Locate every Plasmodium parasite.
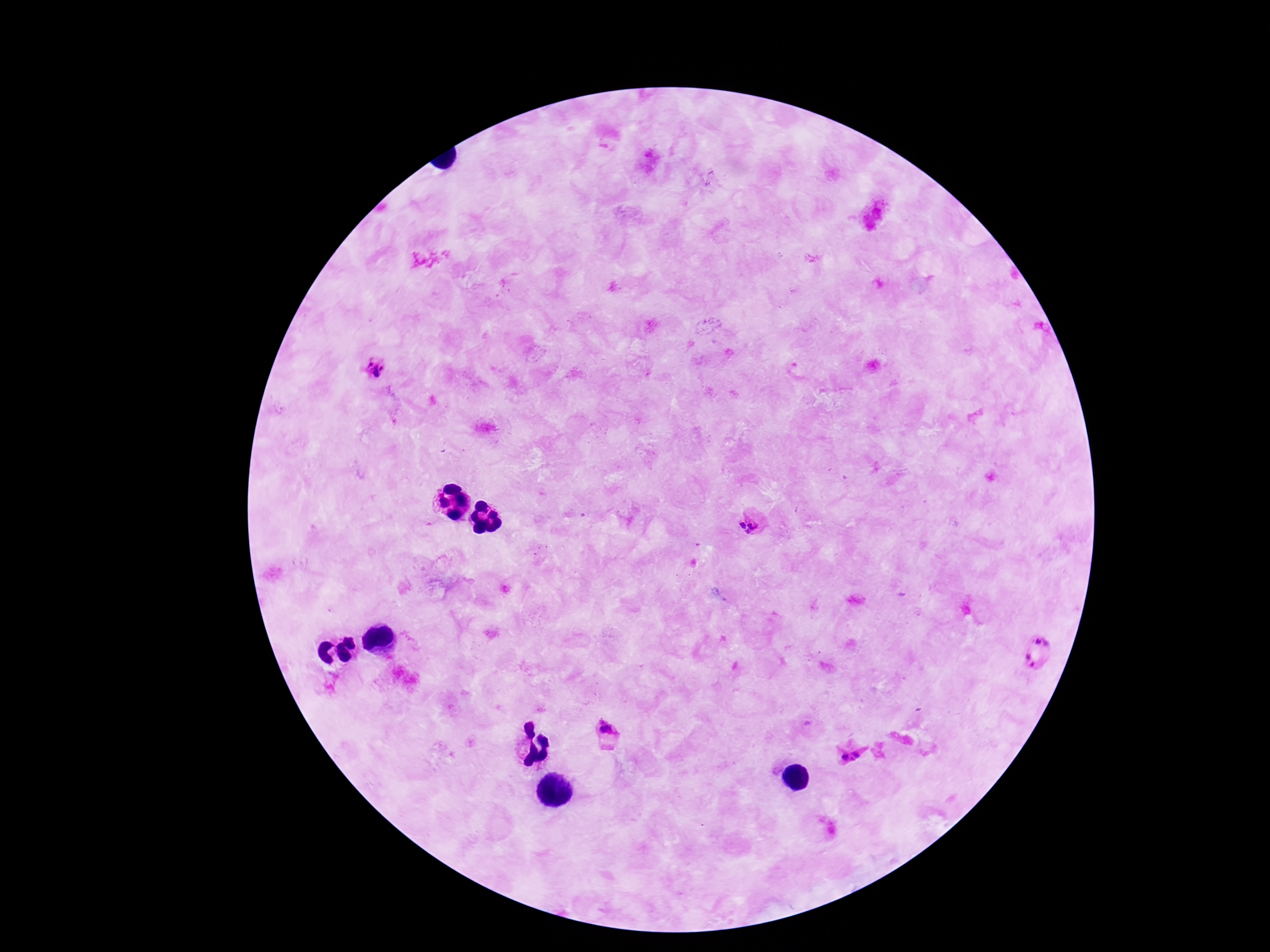

Approximate object centers, in pixels from the top-left corner.
Plasmodium parasites: (x=374, y=368), (x=749, y=525), (x=1044, y=638), (x=1032, y=662), (x=607, y=730), (x=856, y=754), (x=845, y=756), (x=852, y=760).

Summary:
  - Capture: smartphone camera through the microscope eyepiece
  - Magnification: 100x
  - Patient malaria status: infected
  - Field of view: single
  - Preparation: thick peripheral-blood smear
  - Image size: 1270×952 pixels
  - Stain: Giemsa